Draw a bounding box around every parasitised red blood cell.
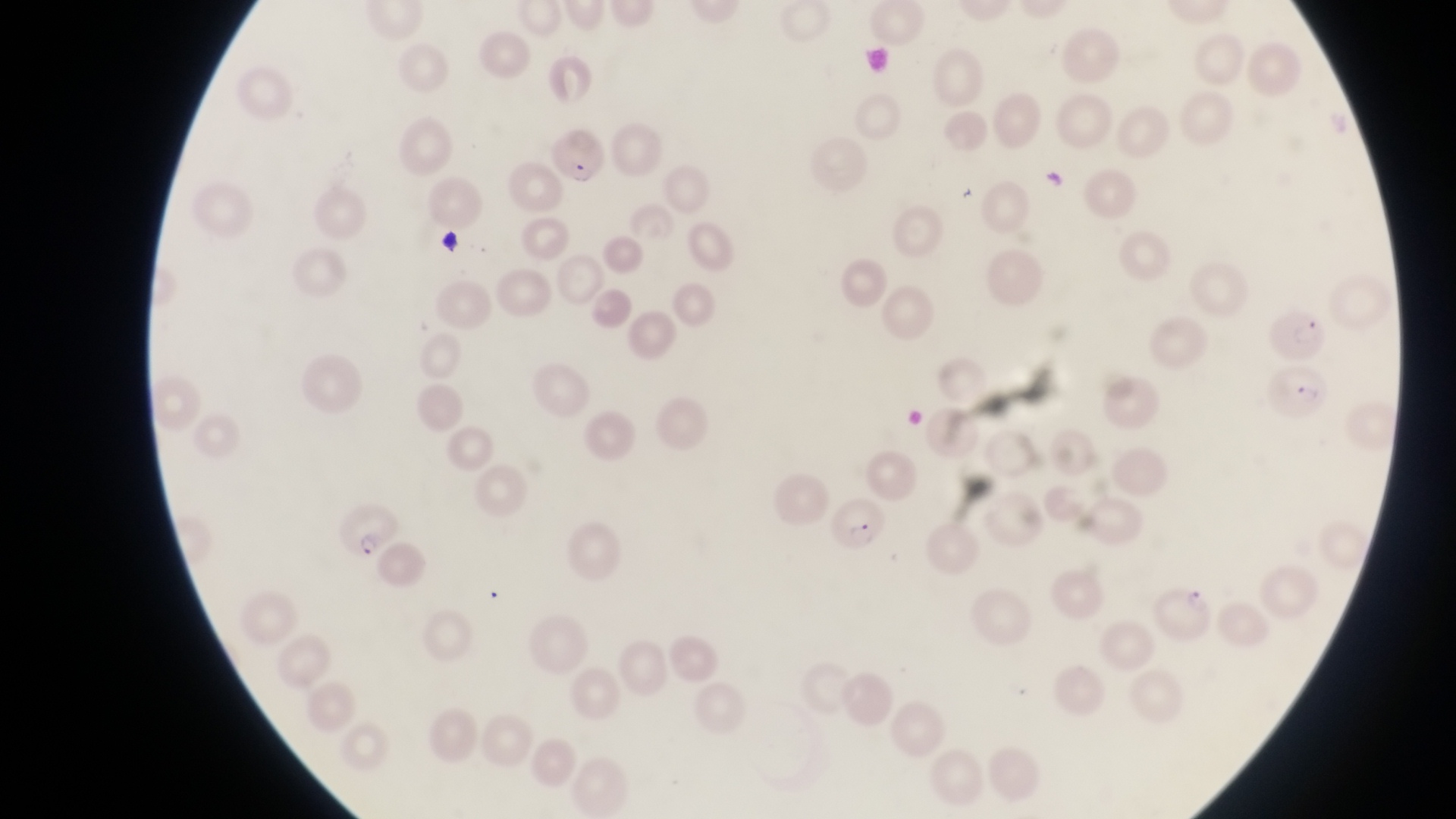
Approximate bounding boxes as left top right bottom in pixels.
Parasitised red blood cells: 551 133 607 183; 1265 301 1332 367; 1266 364 1327 428; 836 495 888 556; 330 500 401 556; 1156 581 1216 640.

Summary:
  - Field of view: single
  - Country: Uganda
  - Capture: smartphone photograph through the eyepiece of an Olympus CX-23 microscope
  - Magnification: 1000x
  - Preparation: thin blood smear
  - Image size: 1456×819 pixels